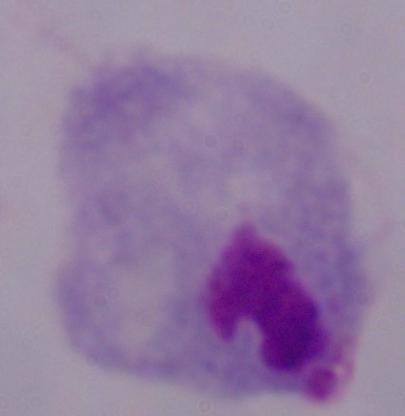

Summary:
  - Modality: micrograph
  - Identification: trichomonad
  - Magnification: 1000x